Classify this cell by malaria status.
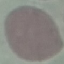

It is uninfected.

image type = cell patch, automatically extracted from a larger field of view and resized to 64 × 64 pixels
stain = Giemsa
preparation = thin blood smear
capture = smartphone camera at the microscope eyepiece